State which parasite is depicted.
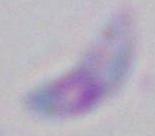
Toxoplasma gondii.

modality = photomicrograph
magnification = 1000x